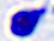
magnification = 400x
identification = white blood cell
modality = photomicrograph